Name the cell type shown.
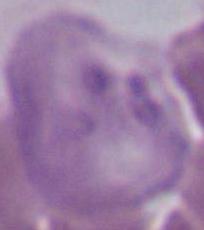

This is an erythrocyte.

magnification = 1000x
modality = photomicrograph